Give the extent of all Plasmodium ovale-infected red blood cells.
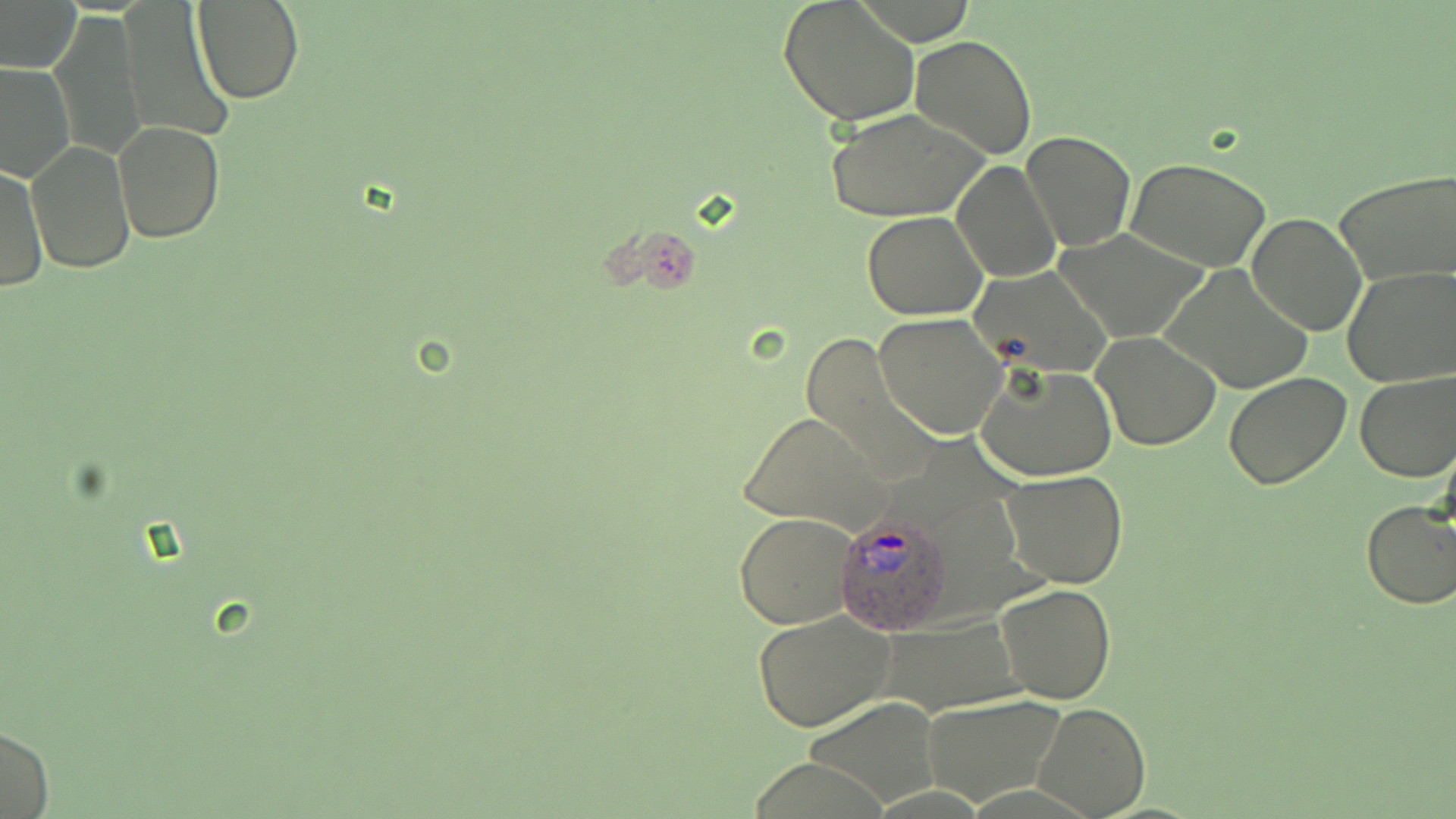
Approximate bounding boxes as (x1, y1, x2, y2) in pixels.
Plasmodium ovale-infected red blood cells: (832, 512, 953, 634).

slide-level diagnosis = Plasmodium ovale
preparation = thin blood smear
magnification = 1000x
stain = May-Grünwald-Giemsa
field of view = single
image size = 1456×819 pixels
modality = optical microscopy
uninfected red blood cell locations = approximate bounding boxes as (x1, y1, x2, y2) in pixels: (777, 0, 920, 127), (192, 1, 304, 104), (0, 2, 80, 72), (119, 5, 231, 140), (48, 13, 146, 161), (910, 35, 1037, 159), (927, 36, 1046, 281), (0, 62, 77, 183), (827, 107, 992, 223), (114, 120, 226, 241), (1021, 131, 1134, 252), (26, 139, 135, 272), (1126, 157, 1273, 270), (952, 159, 1062, 283), (1, 163, 47, 291), (1335, 171, 1456, 286), (862, 211, 987, 321), (1245, 211, 1367, 337), (1053, 227, 1214, 343), (1157, 263, 1317, 395), (971, 265, 1113, 375), (1339, 265, 1456, 386), (875, 313, 1007, 441), (798, 332, 928, 471), (1091, 332, 1223, 452), (976, 362, 1116, 482), (1353, 369, 1456, 482), (1224, 373, 1352, 490), (742, 413, 890, 531), (999, 469, 1129, 589), (1359, 501, 1456, 609), (734, 512, 858, 629), (995, 582, 1116, 704), (752, 611, 895, 731), (881, 619, 1027, 715), (804, 694, 944, 808), (922, 694, 1067, 807), (1030, 701, 1150, 817), (0, 725, 55, 817)